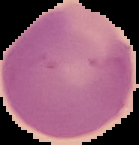 Image is 139×145 pixels. The area outside the segmented cell region is set to black. Malaria status: uninfected. From a thin blood film.